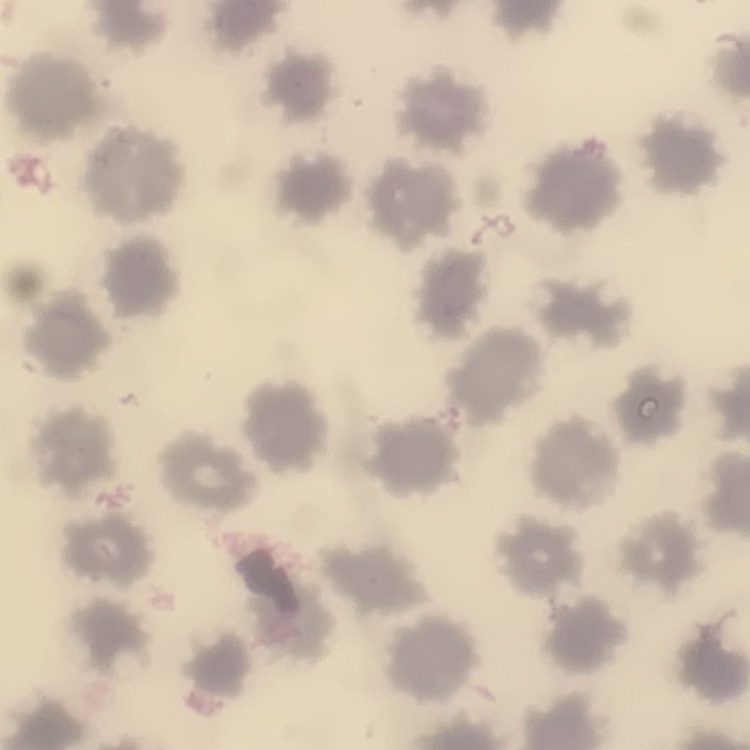

erythrocyte morphology = no rouleaux formation
stain = Field's or Giemsa
preparation = thin peripheral smear
image type = one tile cut from a larger photomicrograph